Report the malaria status of this cell.
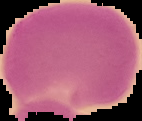
It is uninfected.

preparation: thin blood smear
image_size: 142×121 pixels
image_type: cell region segmented out of the field of view; surrounding area masked to black